Locate every Plasmodium parasite.
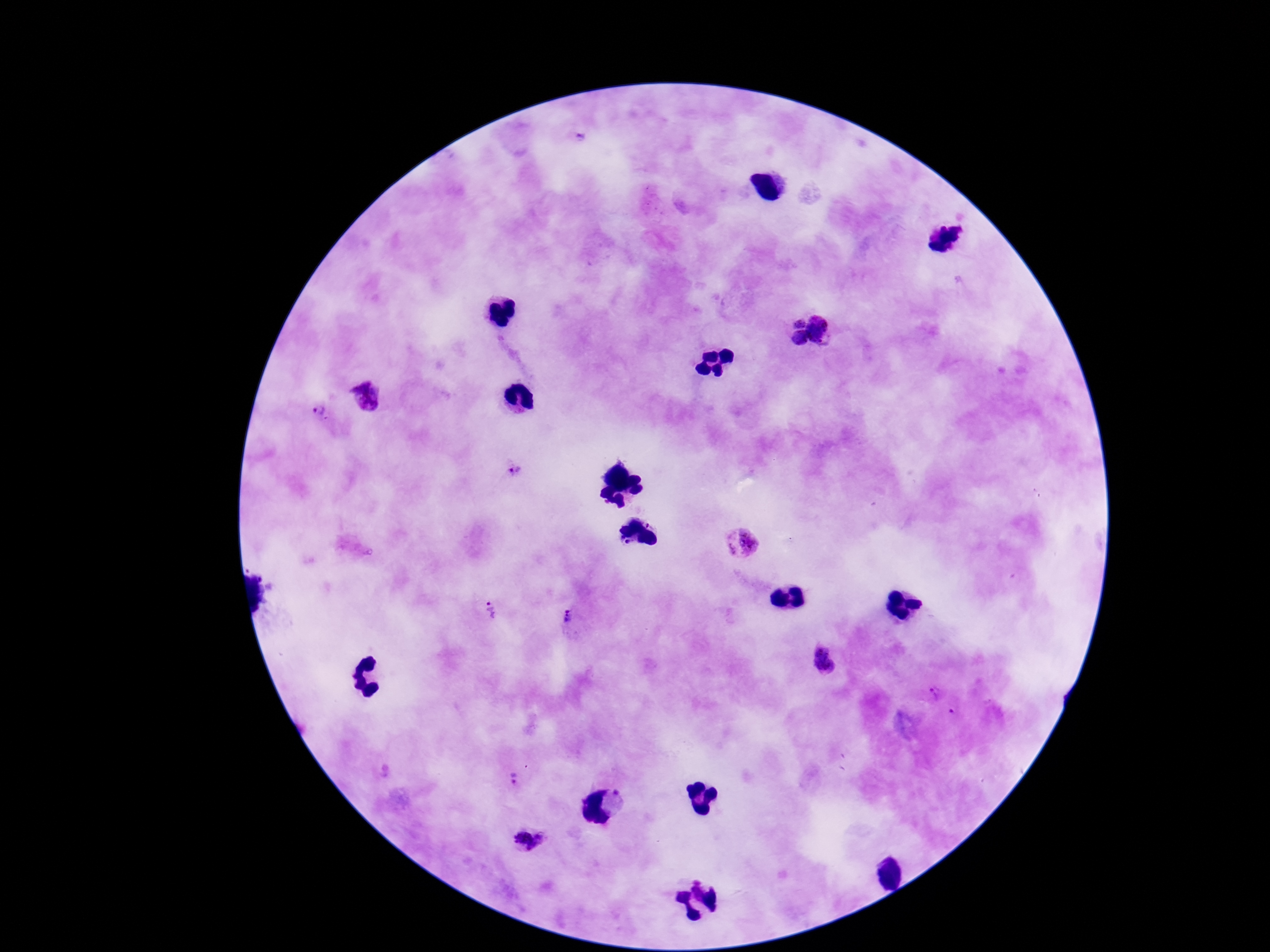

Approximate centers as {x, y} in pixels.
Plasmodium parasites: {367, 397}, {317, 409}, {514, 470}, {744, 542}, {493, 611}, {568, 618}, {824, 661}, {935, 693}, {954, 712}, {517, 780}, {525, 840}.

image_size: 1270×952 pixels
field_of_view: one from this slide
magnification: 100x
patient_malaria_status: positive
capture: smartphone camera through the microscope eyepiece
stain: Giemsa
preparation: thick peripheral-blood smear